State which parasite is depicted.
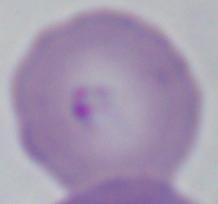

This is Babesia.

Captured at 1000x magnification. Micrograph.